Assess the morphology of the erythrocytes.
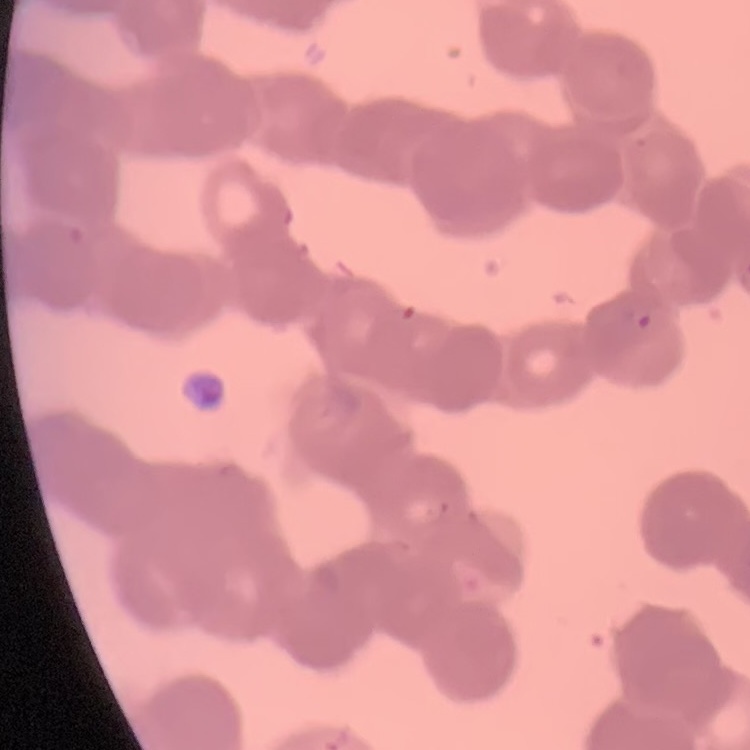
Rouleaux formation.

Summary:
  - Image type: square crop of a larger photomicrograph
  - Preparation: thin peripheral smear
  - Stain: Field's or Giemsa